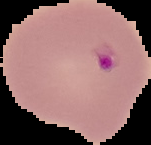
Image is 151×145 pixels. Result: Plasmodium parasites detected. Cell region segmented out of the field of view; the surrounding area is masked to black. From a thin blood film.